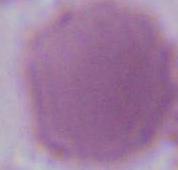

Summary:
  - Modality: photomicrograph
  - Identification: erythrocyte
  - Magnification: 1000x